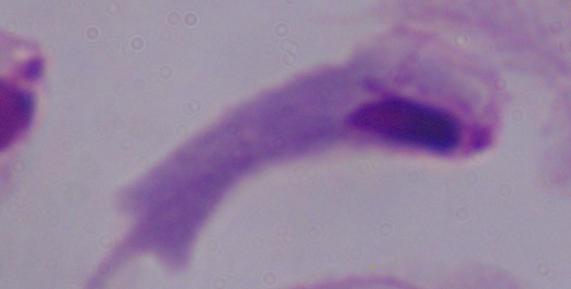

Summary:
  - Modality: photomicrograph
  - Magnification: 1000x
  - Identification: trichomonad